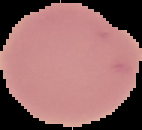 Image is 142×130 pixels. From a thin blood film. Cell region segmented out of the field of view; the surrounding area is masked to black. Malaria status: uninfected.